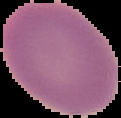

Image is 121×118 pixels. The area outside the segmented cell region is set to black. Result: negative for malaria parasites. From a thin blood smear.